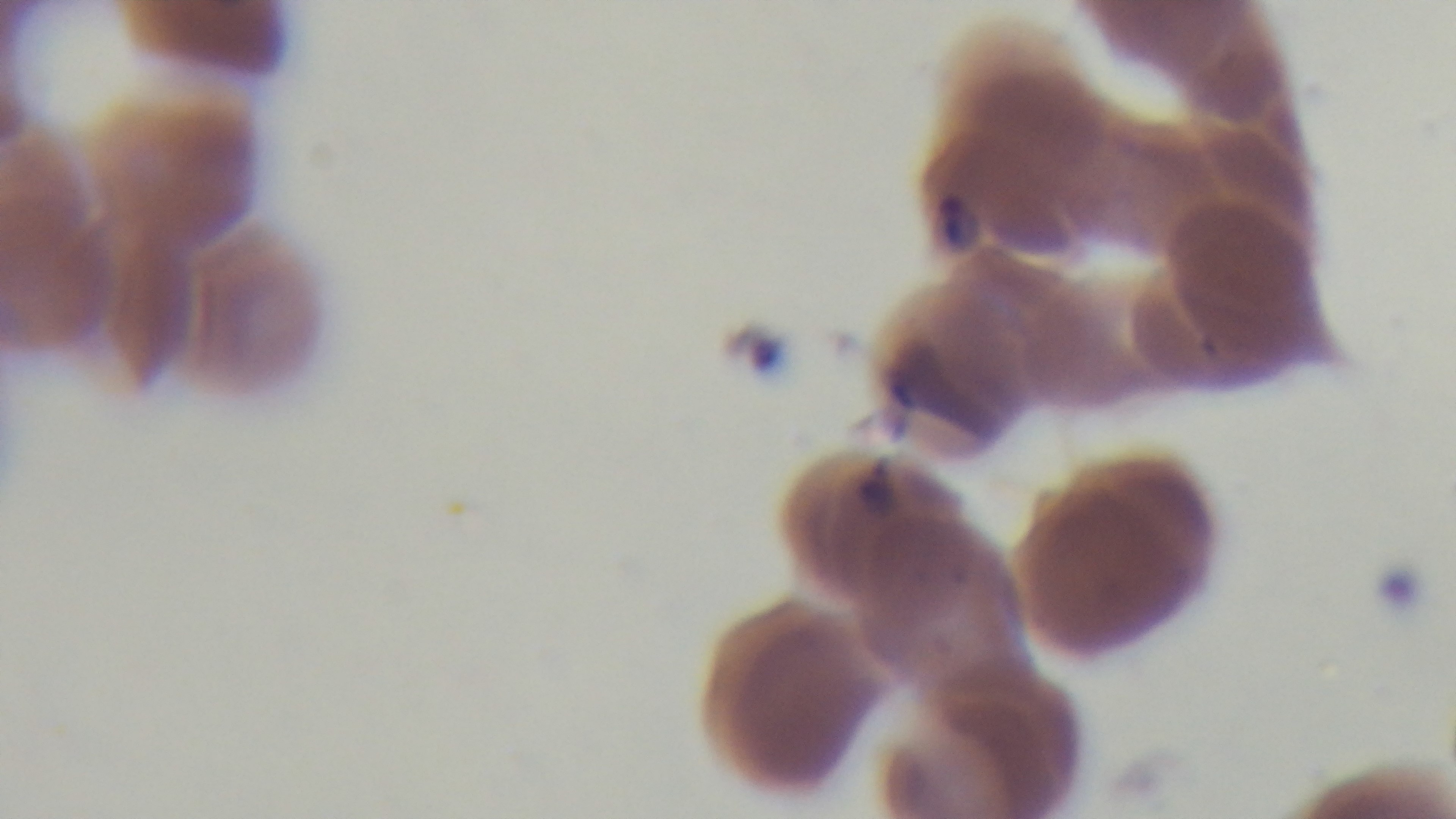
Summary:
  - Capture: mounted 4K digital camera
  - Field of view: one from the slide
  - Objective: 100x oil immersion
  - Malaria status: positive
  - Modality: light microscopy
  - Stain: Giemsa
  - Preparation: thin